Comment on the morphology of the red blood cells.
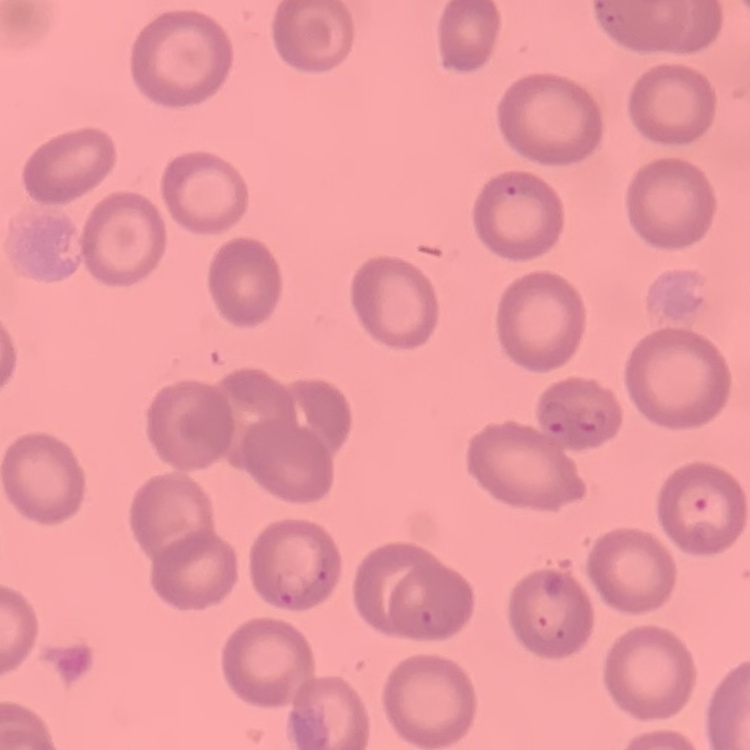
They show no rouleaux formation.

Summary:
  - Image type: one tile cut from a larger photomicrograph
  - Preparation: thin blood film
  - Stain: Field's or Giemsa